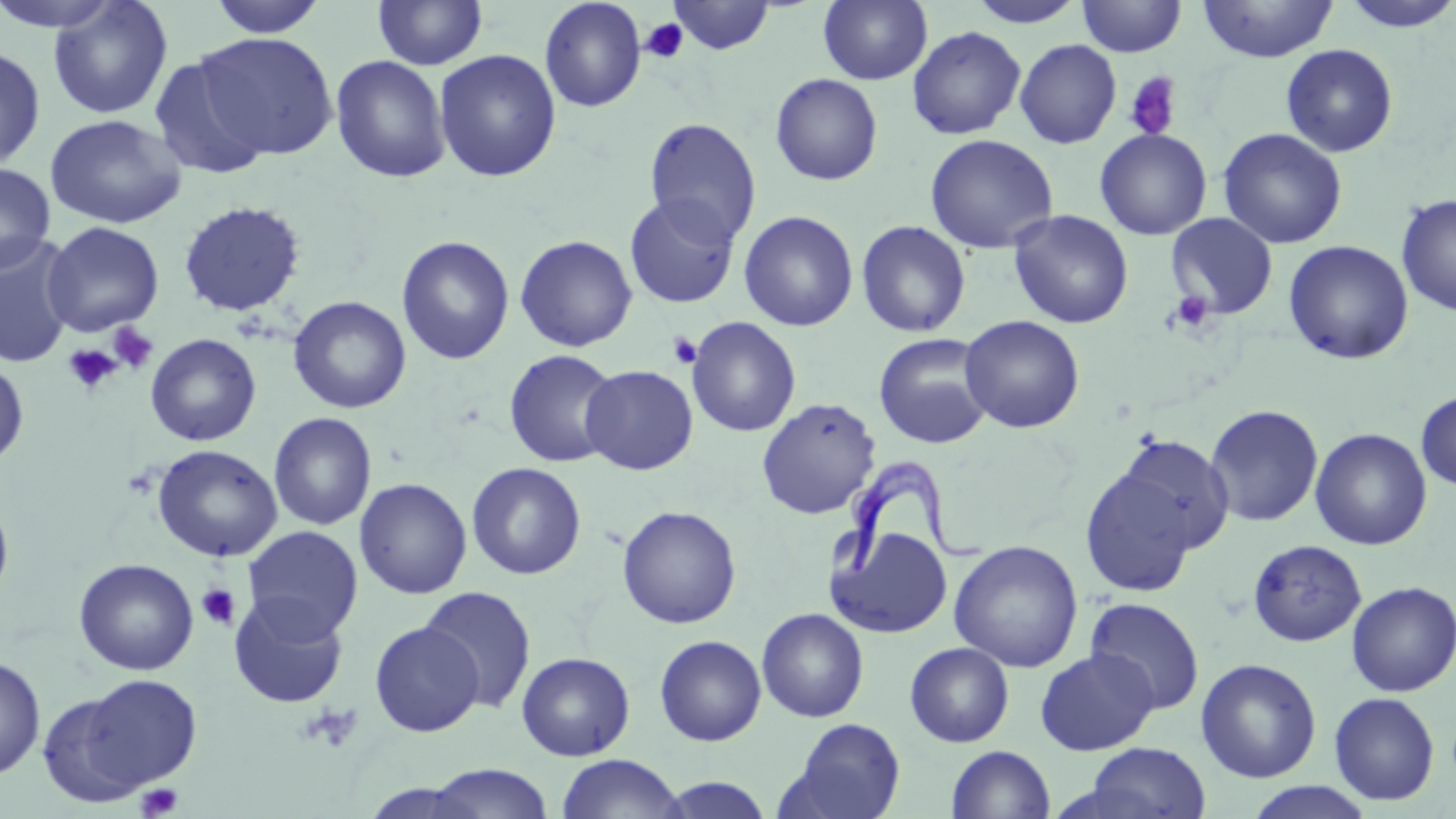
{
  "slide_level_diagnosis": "Trypanosoma brucei",
  "magnification": "1000x",
  "uninfected_red_blood_cell_locations": "approximate bounding boxes as [x1, y1, x2, y2] in pixels: [0, 0, 126, 32], [206, 0, 329, 37], [372, 0, 488, 70], [539, 0, 647, 113], [667, 0, 776, 55], [819, 0, 932, 85], [1076, 0, 1187, 57], [1198, 0, 1338, 63], [1338, 0, 1456, 33], [47, 1, 173, 120], [966, 1, 1086, 28], [907, 25, 1027, 140], [194, 33, 338, 160], [1014, 39, 1122, 149], [1280, 44, 1398, 157], [0, 45, 46, 173], [434, 49, 561, 182], [148, 52, 271, 181], [330, 54, 451, 183], [769, 73, 883, 185], [44, 114, 186, 229], [643, 116, 761, 245], [1218, 127, 1347, 250], [1094, 128, 1212, 240], [924, 133, 1059, 254], [0, 162, 56, 274], [1396, 193, 1456, 317], [624, 194, 740, 309], [178, 200, 305, 317], [1008, 209, 1134, 329], [739, 210, 859, 331], [1166, 212, 1279, 320], [855, 220, 971, 338], [42, 222, 164, 337], [0, 235, 77, 369], [396, 235, 514, 365], [515, 235, 637, 352], [1283, 240, 1414, 365], [288, 296, 411, 414], [960, 315, 1084, 433], [686, 316, 800, 437], [145, 333, 261, 446], [873, 333, 994, 449], [503, 349, 620, 468], [0, 356, 29, 468], [580, 365, 698, 475], [1415, 390, 1456, 490], [756, 397, 881, 519], [1204, 404, 1324, 527], [268, 412, 377, 531], [1310, 427, 1432, 550], [1112, 434, 1235, 555], [151, 443, 283, 562], [466, 462, 586, 580], [1079, 464, 1200, 597], [354, 478, 472, 599], [0, 492, 15, 610], [617, 505, 742, 629], [828, 524, 952, 639], [242, 526, 363, 642], [1247, 539, 1367, 647], [948, 540, 1084, 672], [74, 558, 199, 676], [1345, 581, 1456, 697], [419, 585, 536, 713], [228, 594, 348, 709], [1085, 598, 1206, 714], [756, 608, 869, 723], [369, 621, 484, 737], [654, 634, 766, 746], [904, 641, 1014, 748], [1034, 648, 1160, 755], [517, 652, 635, 761], [0, 656, 46, 781], [1196, 658, 1322, 783], [77, 673, 203, 792], [37, 691, 151, 806], [1329, 691, 1440, 806], [782, 717, 907, 819], [1082, 742, 1211, 818], [946, 745, 1055, 819], [556, 754, 686, 818], [423, 764, 555, 819], [656, 776, 775, 818], [1243, 782, 1377, 819]",
  "trypanosoma_brucei_locations": "approximate bounding boxes as [x1, y1, x2, y2] in pixels: [833, 455, 986, 578]",
  "modality": "light microscopy",
  "preparation": "thin blood smear",
  "field_of_view": "single",
  "stain": "May-Grünwald-Giemsa",
  "platelet_locations": "approximate bounding boxes as [x1, y1, x2, y2] in pixels: [639, 18, 688, 64], [1122, 72, 1183, 141], [1168, 290, 1216, 333], [107, 324, 159, 374], [667, 331, 702, 369], [63, 344, 122, 396], [195, 583, 242, 630], [298, 703, 364, 754], [136, 782, 183, 818]",
  "image_size": "1456×819 pixels"
}